Classify this cell by malaria status.
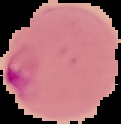

It is parasitized.

preparation: thin blood smear
image_type: segmented cell region on a black background
image_size: 121×124 pixels